State which parasite is depicted.
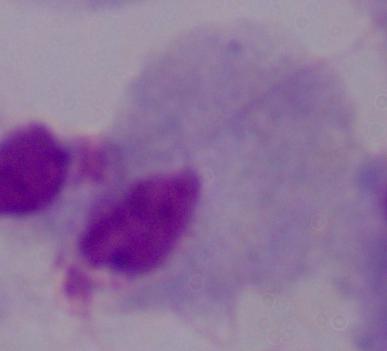

A trichomonad.

modality = photomicrograph
magnification = 1000x